Assess this cell for malaria.
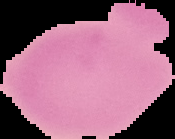
It is uninfected.

Summary:
  - Preparation: thin blood film
  - Image size: 175×139 pixels
  - Image type: segmented cell region on a black background